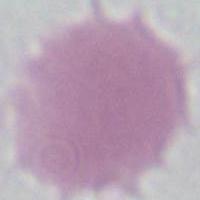
Photomicrograph. 1000x magnification. A red blood cell is shown.